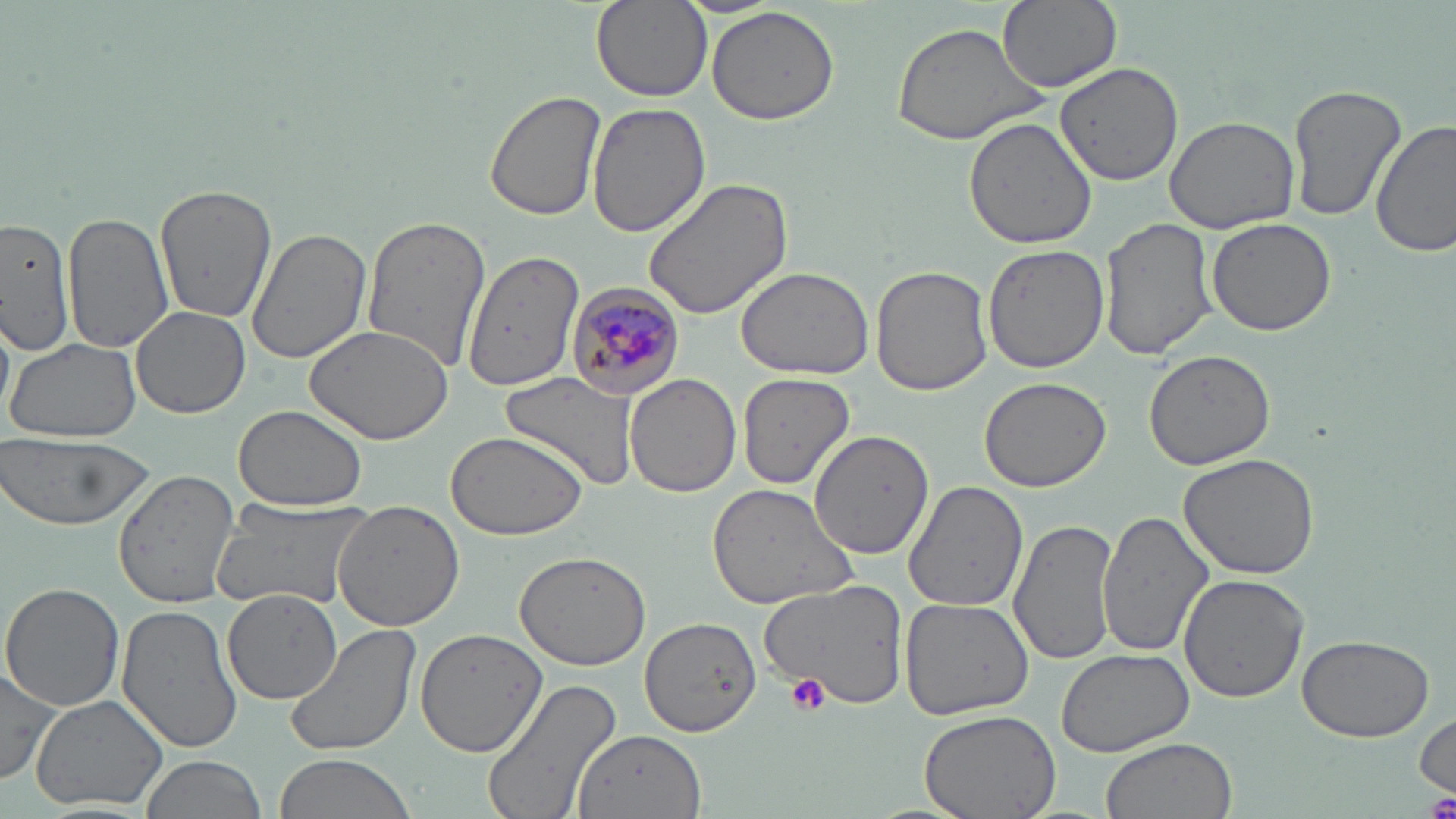
slide_level_diagnosis: Plasmodium malariae
uninfected_red_blood_cell_locations: 'approximate bounding boxes as (x1,y1)-(x2,y2) corner pairs in pixels: (590,0)-(711,102), (997,0)-(1121,91), (705,5)-(843,128), (889,20)-(1052,148), (1055,61)-(1183,186), (1287,84)-(1404,225), (485,90)-(603,222), (587,100)-(710,236), (962,115)-(1097,251), (1164,116)-(1300,235), (1371,119)-(1455,260), (641,176)-(794,321), (152,182)-(277,326), (63,213)-(172,358), (1098,214)-(1217,361), (360,215)-(492,373), (0,216)-(75,356), (1206,216)-(1336,336), (246,228)-(371,365), (985,243)-(1107,372), (461,244)-(580,402), (735,265)-(877,380), (872,265)-(994,395), (132,306)-(249,418), (304,326)-(453,442), (6,337)-(142,443), (1143,349)-(1277,469), (501,371)-(639,489), (738,372)-(857,491), (625,374)-(740,497), (979,377)-(1111,492), (233,404)-(368,513), (810,428)-(933,558), (445,430)-(587,540), (0,433)-(154,532), (1177,449)-(1321,579), (113,467)-(240,609), (905,480)-(1030,613), (707,483)-(861,611), (212,496)-(374,614), (332,499)-(467,631), (1096,506)-(1217,658), (1011,518)-(1121,667), (514,551)-(652,671), (1177,573)-(1308,703), (755,581)-(908,704), (2,582)-(125,713), (222,590)-(345,706), (899,596)-(1034,720), (116,603)-(242,754), (640,616)-(763,736), (283,622)-(421,759), (414,628)-(545,758), (1298,634)-(1434,742), (1056,648)-(1194,758), (0,663)-(62,788), (481,675)-(623,819), (31,694)-(169,812), (917,706)-(1062,819), (1414,710)-(1454,800), (573,727)-(707,819), (1100,738)-(1237,819), (273,754)-(416,819), (139,755)-(265,819)'
image_size: 1456×819 pixels
stain: May-Grünwald-Giemsa
modality: light microscopy
plasmodium_malariae_infected_red_blood_cell_locations: 'approximate bounding boxes as (x1,y1)-(x2,y2) corner pairs in pixels: (565,280)-(688,399)'
field_of_view: one of a larger specimen
magnification: 1000x
preparation: thin blood smear
platelet_locations: 'approximate bounding boxes as (x1,y1)-(x2,y2) corner pairs in pixels: (786,673)-(829,715), (1422,792)-(1456,819)'